Assess this cell for malaria.
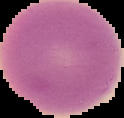

Uninfected.

image size = 124×118 pixels
preparation = thin blood film
image type = segmented cell region on a black background